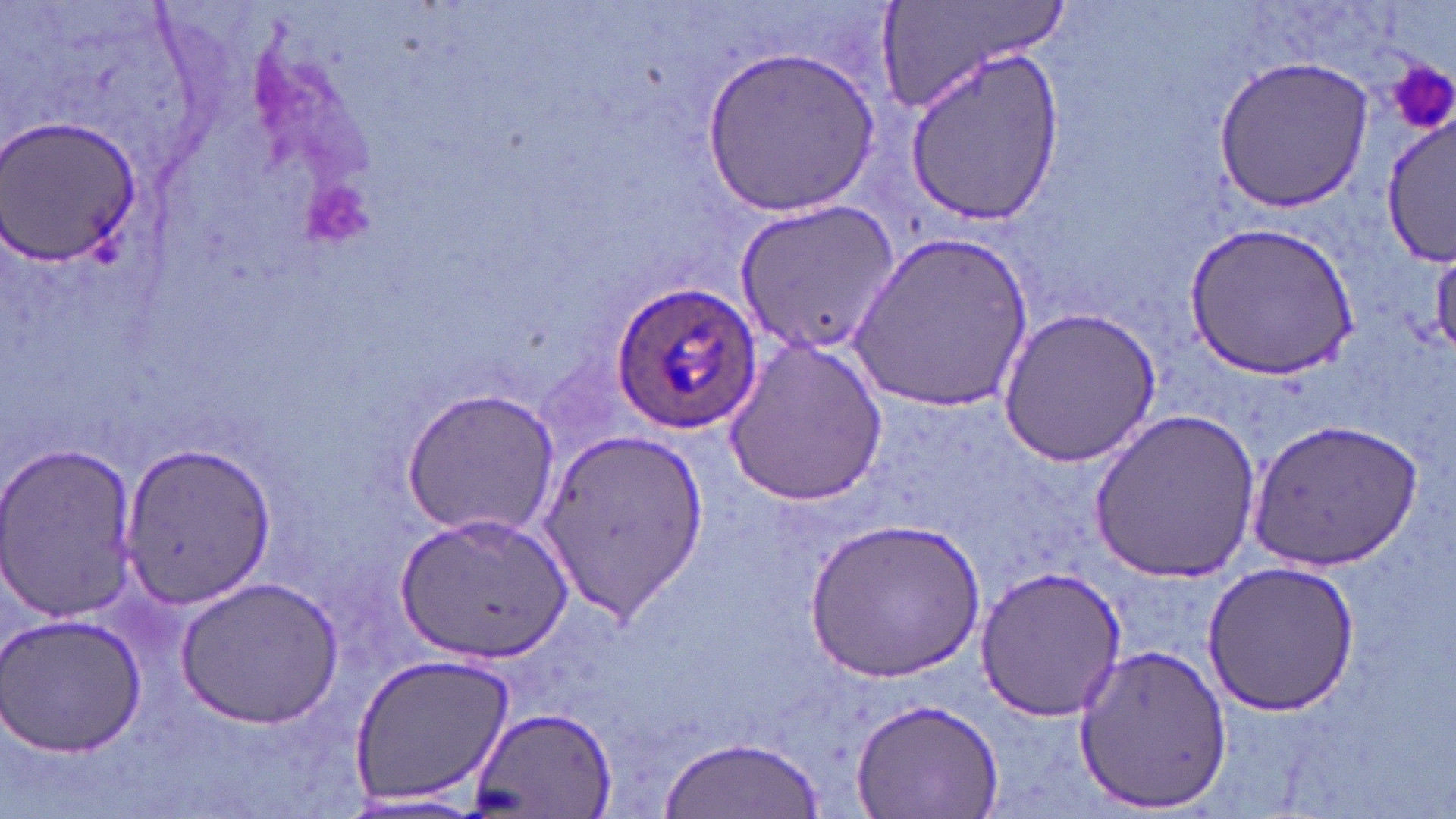

slide-level diagnosis = Plasmodium ovale
field of view = single
uninfected red blood cell locations = approximate bounding boxes as (x1, y1, x2, y2) in pixels: (875, 2, 1067, 117), (698, 45, 880, 217), (902, 47, 1064, 229), (1214, 56, 1375, 211), (1381, 115, 1454, 268), (1, 117, 142, 264), (735, 198, 898, 354), (1185, 220, 1358, 379), (849, 230, 1034, 415), (997, 308, 1161, 465), (724, 333, 888, 507), (398, 386, 560, 536), (1089, 409, 1266, 582), (1247, 417, 1422, 571), (541, 427, 707, 620), (119, 440, 275, 609), (0, 442, 139, 624), (397, 509, 573, 663), (807, 518, 984, 682), (1200, 559, 1361, 716), (973, 565, 1127, 720), (174, 577, 344, 727), (2, 610, 148, 761), (1070, 644, 1235, 814), (348, 651, 516, 810), (853, 697, 1005, 819), (469, 707, 615, 819), (658, 733, 821, 815), (334, 793, 493, 818)
image size = 1456×819 pixels
magnification = 1000x
preparation = thin blood film
platelet locations = approximate bounding boxes as (x1, y1, x2, y2) in pixels: (1386, 56, 1455, 131)
stain = May-Grünwald-Giemsa
Plasmodium ovale-infected red blood cell locations = approximate bounding boxes as (x1, y1, x2, y2) in pixels: (611, 280, 762, 435)
modality = light microscopy